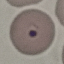

result = malaria parasites detected
capture = smartphone through the microscope eyepiece
image type = automatically extracted cell patch, resized to 64 × 64 pixels
preparation = thin smear
stain = Giemsa